Comment on the morphology of the erythrocytes.
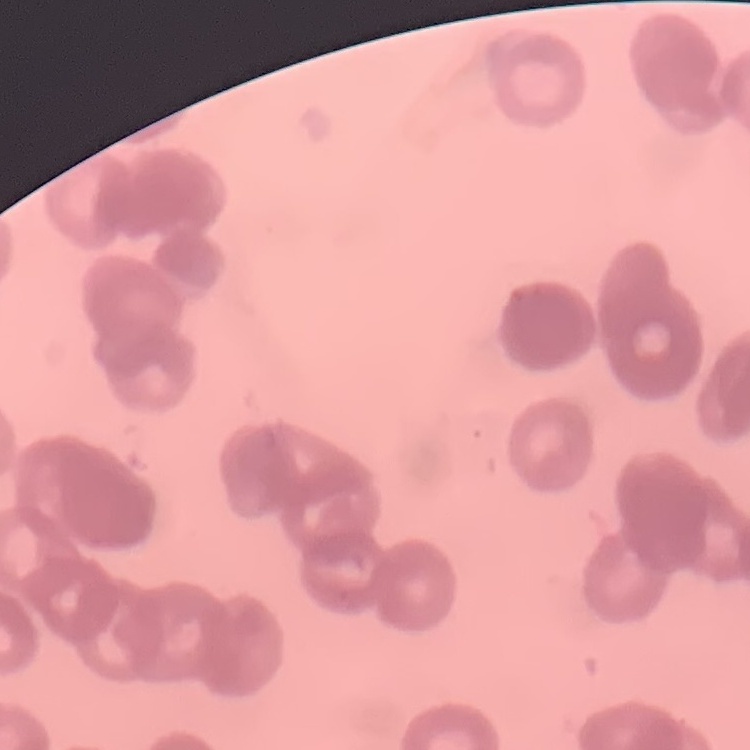

Rouleaux formation.

preparation = thin blood smear
image type = square crop of a larger photomicrograph
stain = Field's or Giemsa